Identify the parasite.
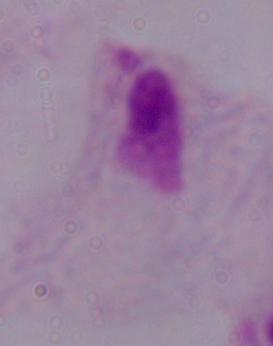

This is a trichomonad.

magnification = 1000x
modality = photomicrograph